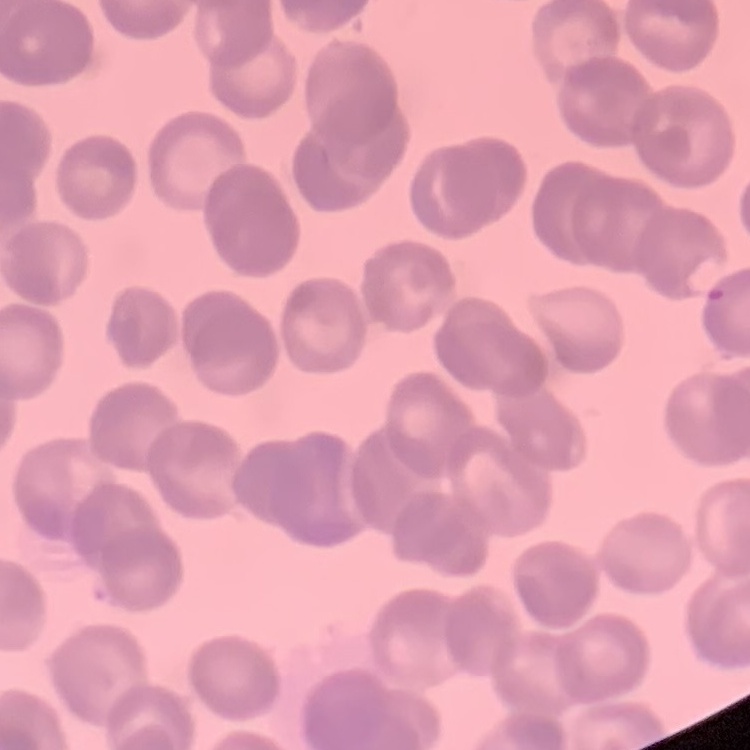
Summary:
  - Erythrocyte morphology: rouleaux formation
  - Stain: Field's or Giemsa
  - Preparation: thin peripheral smear
  - Image type: one tile cut from a larger photomicrograph